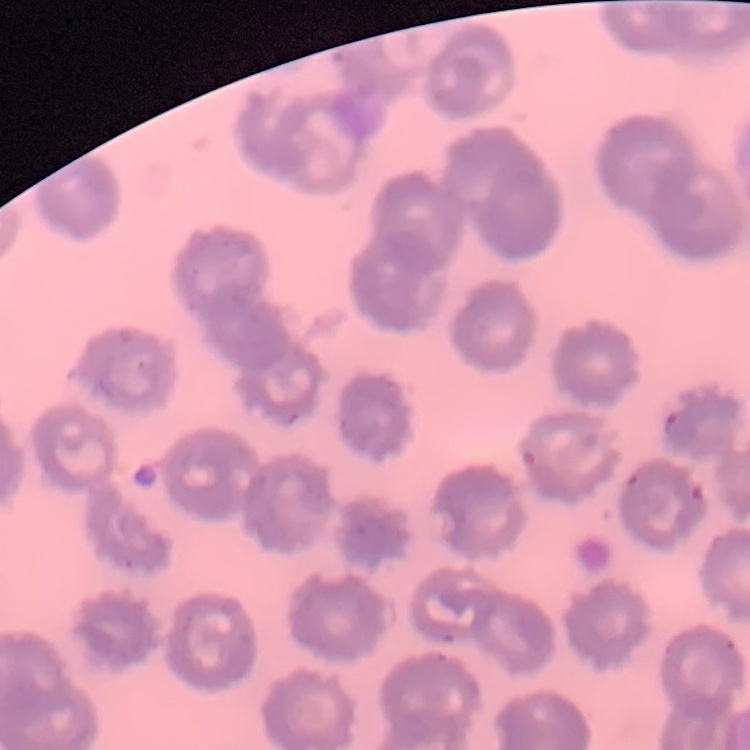
The erythrocytes show no rouleaux formation. Thin blood film. One tile cut from a larger photomicrograph. Stained with either Field's or Giemsa.